Identify the preparation type.
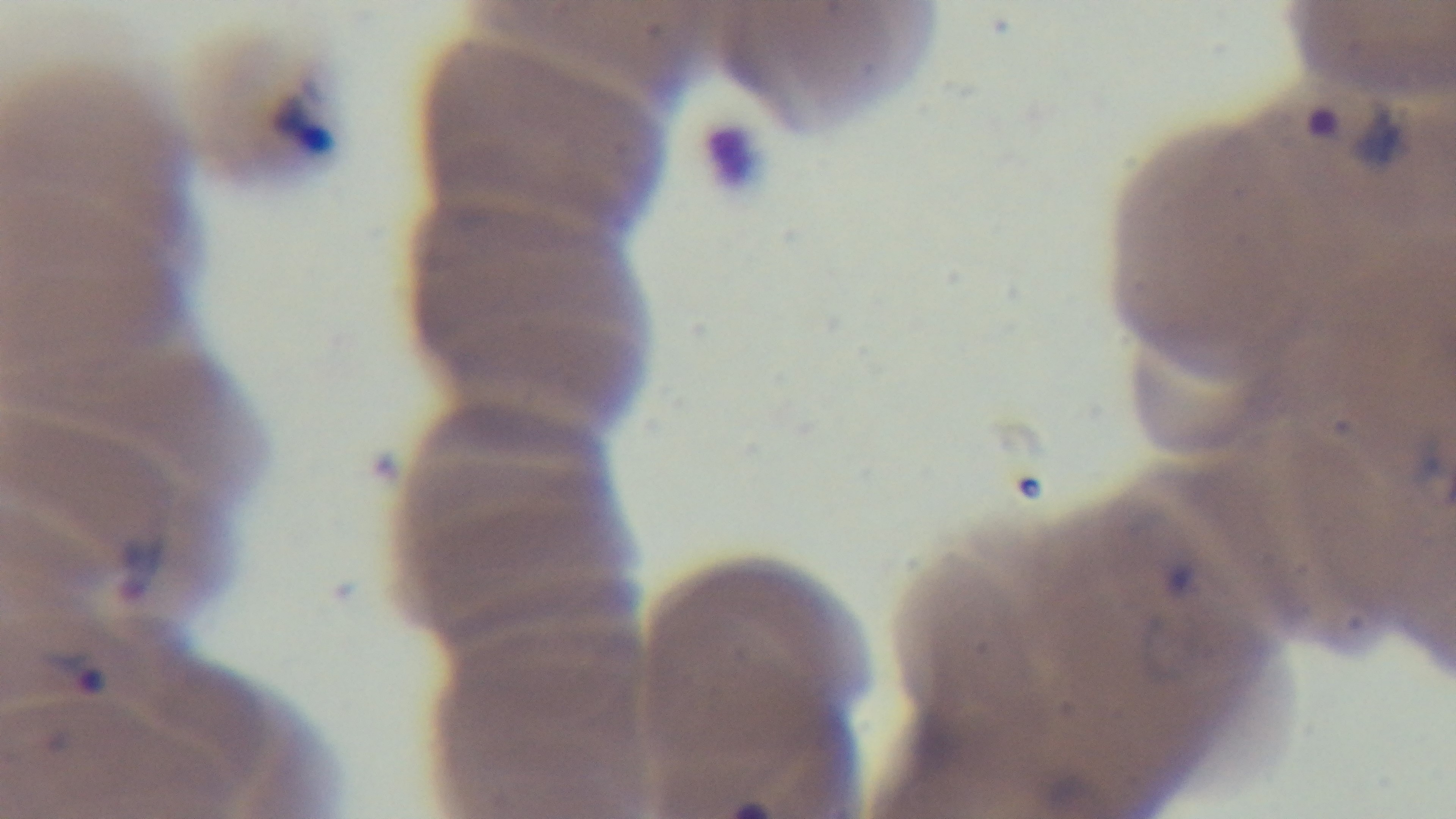
A thin smear.

Summary:
  - Stain: Giemsa
  - Field of view: one from the slide
  - Objective: 100x oil immersion
  - Modality: light microscopy
  - Malaria status: positive
  - Capture: mounted 4K digital camera